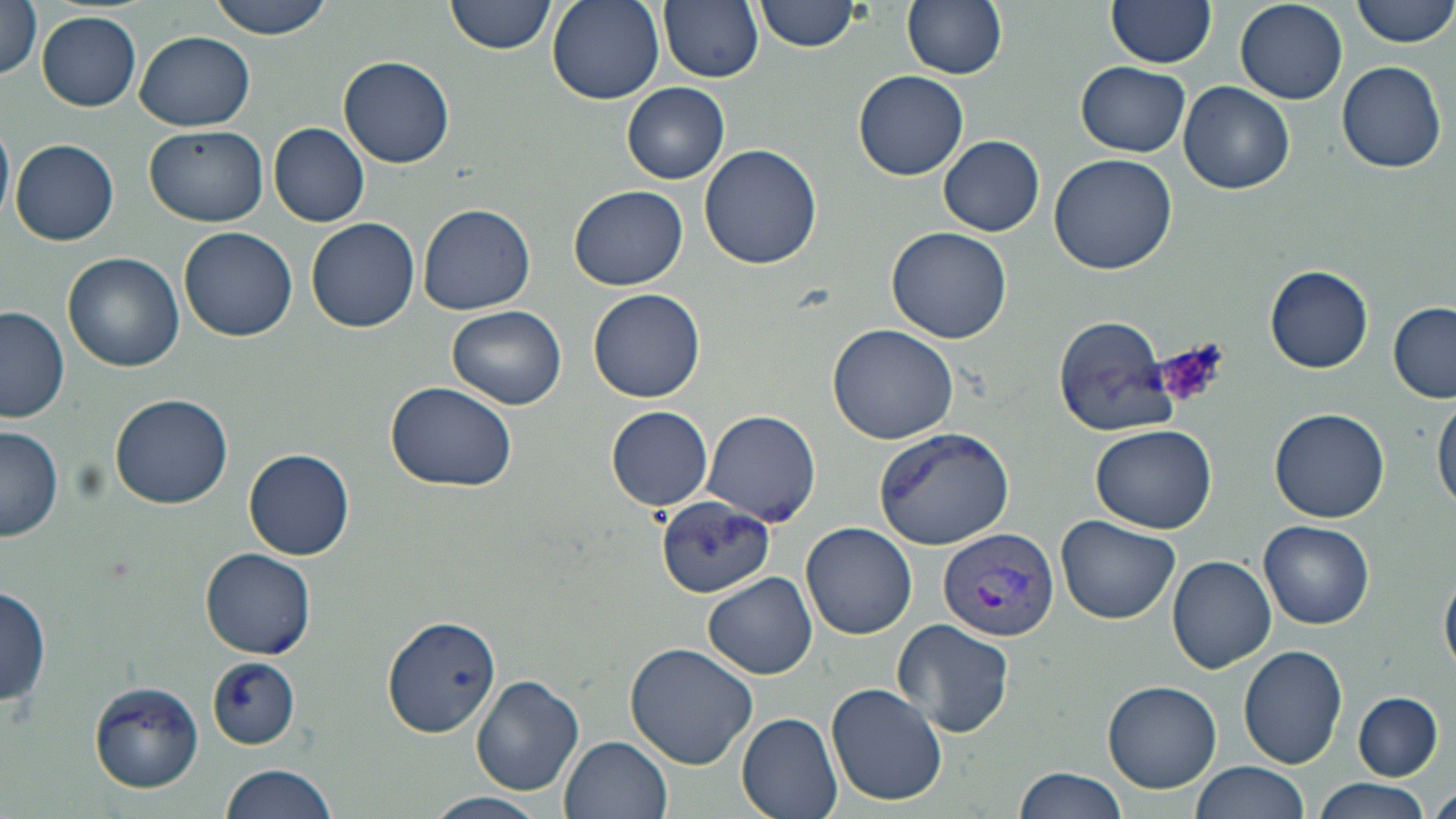 Approximate bounding boxes as (x1, y1, x2, y2) in pixels. Platelet locations: (1158, 340, 1228, 409). Uninfected red blood cell locations: (206, 0, 335, 39), (447, 0, 556, 55), (660, 0, 763, 83), (901, 0, 1008, 80), (1107, 0, 1216, 69), (1352, 0, 1456, 48), (1, 1, 45, 82), (548, 1, 664, 105), (755, 1, 864, 53), (1234, 2, 1349, 106), (37, 12, 140, 110), (133, 32, 256, 130), (338, 56, 456, 168), (1075, 60, 1191, 157), (1337, 61, 1446, 173), (852, 69, 969, 181), (622, 82, 730, 184), (1179, 83, 1295, 195), (0, 118, 14, 228), (269, 124, 369, 227), (146, 126, 268, 226), (939, 135, 1045, 236), (10, 138, 119, 246), (699, 142, 823, 269), (1049, 153, 1179, 275), (569, 185, 687, 289), (417, 204, 537, 316), (306, 216, 421, 333), (179, 226, 298, 342), (886, 227, 1013, 345), (63, 252, 183, 372), (1264, 264, 1375, 373), (589, 288, 706, 402), (1386, 300, 1456, 402), (447, 305, 568, 411), (0, 306, 71, 423), (1053, 314, 1176, 437), (828, 323, 960, 444), (385, 381, 516, 492), (1433, 392, 1456, 516), (110, 394, 234, 510), (606, 405, 716, 510), (1270, 407, 1390, 523), (703, 409, 822, 525), (1088, 422, 1220, 533), (1, 424, 64, 543), (872, 427, 1016, 552), (244, 449, 355, 561), (654, 495, 777, 597), (1056, 514, 1181, 623), (1260, 521, 1374, 630), (803, 522, 918, 641), (201, 547, 316, 660), (1167, 555, 1278, 674), (1440, 563, 1456, 679), (703, 573, 817, 679), (1, 583, 51, 711), (383, 615, 502, 737), (890, 618, 1018, 738), (624, 642, 759, 769), (1239, 645, 1350, 768), (206, 656, 302, 750), (472, 675, 584, 795), (87, 680, 204, 792), (825, 680, 948, 807), (1103, 681, 1222, 793), (1352, 691, 1443, 780), (737, 712, 845, 819), (560, 734, 674, 819), (1192, 760, 1309, 819), (221, 761, 340, 819), (1013, 765, 1127, 819), (1313, 778, 1432, 817), (1430, 786, 1455, 819), (429, 792, 547, 819). Plasmodium vivax-infected red blood cell locations: (939, 526, 1063, 641). Slide-level diagnosis: Plasmodium vivax. Image is 1456×819 pixels. 1000x magnification. Optical microscopy. One field of a larger specimen. Thin blood smear. May-Grünwald-Giemsa stain.